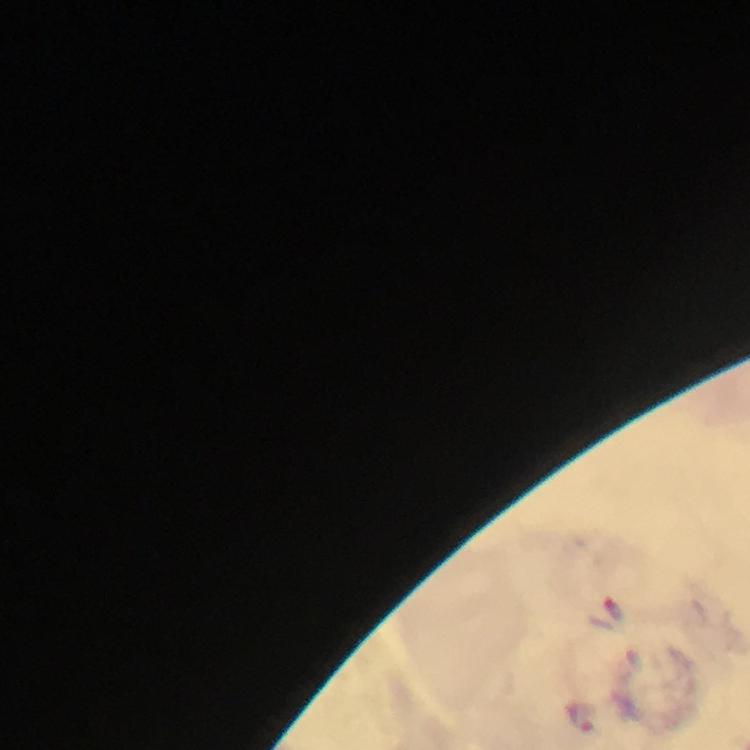

context = from a malaria diagnostic workup
magnification = 100x
cropped from = a single field of view
capture = smartphone mounted on the microscope
preparation = thick blood film
stain = Giemsa
image size = 750×750 pixels
immersion oil = applied
Plasmodium parasite locations = approximate object centers, in pixels from the top-left corner: (x=614, y=608), (x=581, y=714)